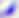

Summary:
  - Modality: micrograph
  - Magnification: 400x
  - Identification: Toxoplasma gondii